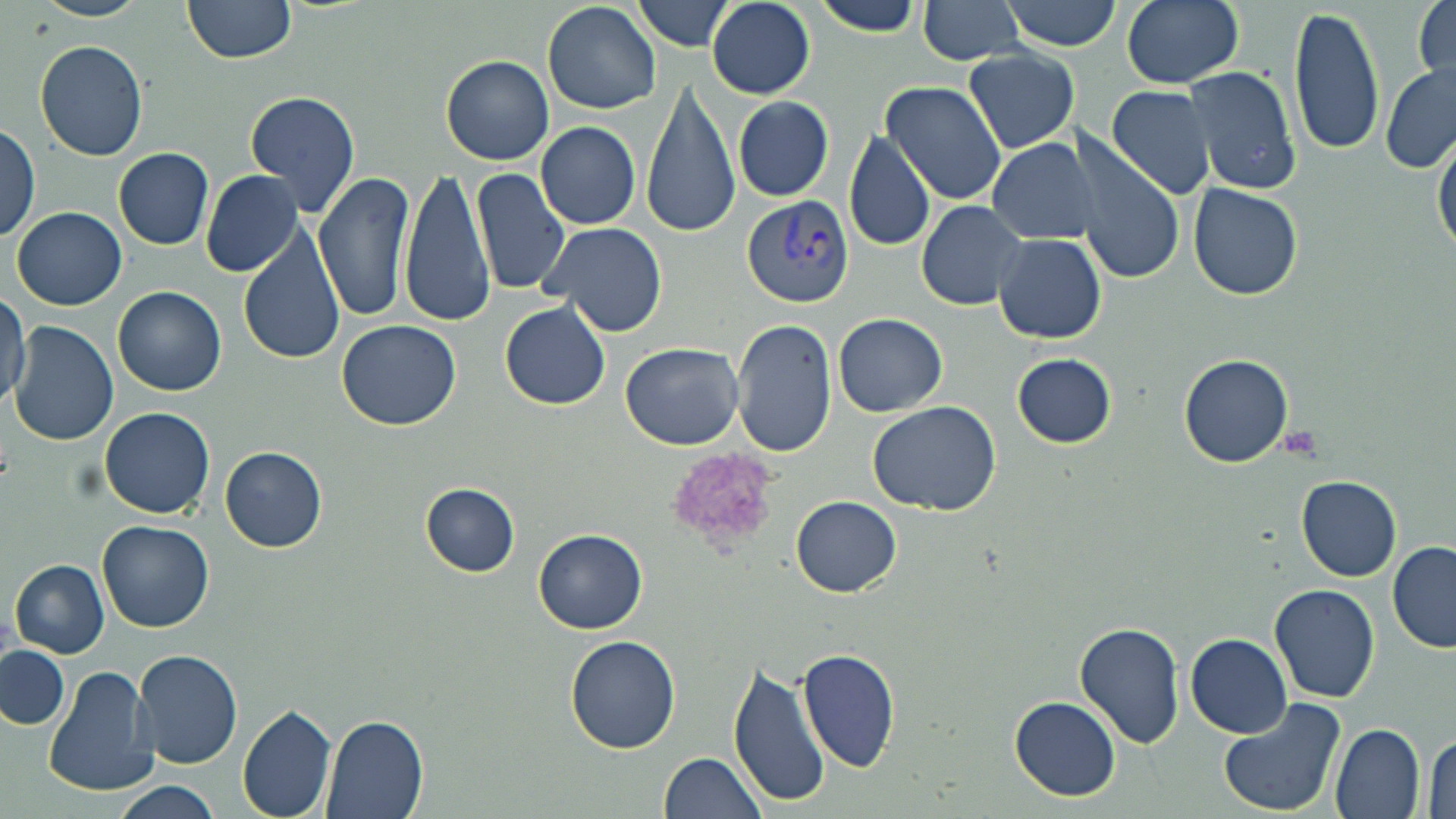
Summary:
  - Coordinate format: approximate bounding boxes as (x1, y1, x2, y2) in pixels
  - Platelet locations: (1277, 428, 1323, 461), (669, 447, 780, 550)
  - Uninfected red blood cell locations: (34, 0, 149, 21), (183, 0, 297, 63), (918, 0, 1030, 64), (1120, 0, 1244, 88), (1414, 0, 1454, 88), (543, 1, 662, 114), (634, 1, 737, 52), (804, 1, 932, 36), (1001, 1, 1125, 51), (706, 3, 815, 99), (1288, 5, 1386, 159), (35, 38, 149, 162), (962, 48, 1079, 153), (441, 54, 555, 165), (1182, 64, 1305, 195), (1381, 65, 1456, 175), (881, 80, 1008, 206), (639, 81, 738, 239), (1107, 85, 1216, 201), (245, 90, 361, 217), (733, 95, 833, 201), (537, 121, 641, 231), (0, 123, 41, 244), (1068, 127, 1184, 284), (1434, 129, 1455, 258), (845, 130, 938, 253), (992, 131, 1127, 339), (987, 138, 1101, 245), (115, 147, 213, 249), (400, 167, 497, 327), (472, 168, 572, 296), (315, 169, 418, 325), (200, 171, 302, 278), (1187, 182, 1303, 301), (916, 199, 1028, 310), (11, 207, 126, 310), (539, 220, 667, 337), (237, 224, 347, 367), (993, 232, 1106, 344), (114, 286, 226, 396), (0, 289, 28, 406), (500, 301, 611, 411), (833, 312, 947, 417), (732, 318, 836, 458), (337, 319, 462, 430), (9, 321, 118, 446), (620, 342, 747, 451), (1010, 352, 1117, 448), (1179, 353, 1294, 467), (867, 399, 1002, 516), (98, 406, 217, 519), (221, 445, 327, 552), (1296, 475, 1401, 581), (419, 483, 521, 576), (791, 496, 901, 598), (98, 521, 214, 633), (535, 529, 646, 633), (1387, 542, 1456, 655), (10, 559, 110, 657), (1268, 583, 1380, 703), (1075, 621, 1186, 749), (1187, 634, 1290, 738), (565, 637, 681, 754), (0, 646, 70, 731), (134, 648, 245, 770), (798, 649, 901, 771), (729, 661, 830, 808), (45, 664, 156, 797), (1010, 695, 1120, 801), (1217, 695, 1346, 819), (237, 703, 338, 819), (319, 712, 428, 819), (1331, 722, 1425, 819), (1424, 733, 1456, 818), (662, 752, 769, 817), (107, 780, 225, 819)
  - Plasmodium vivax-infected red blood cell locations: (740, 195, 854, 312)
  - Slide-level diagnosis: Plasmodium vivax
  - Magnification: 1000x
  - Preparation: thin blood film
  - Stain: May-Grünwald-Giemsa
  - Image size: 1456×819 pixels
  - Field of view: single
  - Modality: optical microscopy